Locate every malaria parasite.
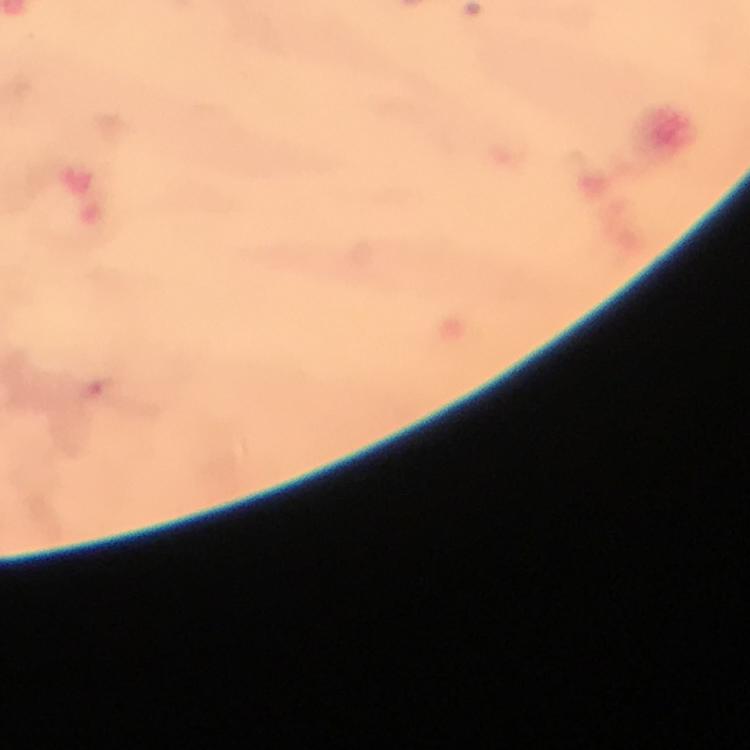

Approximate centers as (x, y) in pixels.
Malaria parasites: (102, 389).

Summary:
  - Magnification: 100x
  - Cropped from: one field of view
  - Preparation: thick blood film
  - Capture: smartphone camera through the microscope
  - Context: from a diagnostic examination for malaria
  - Image size: 750×750 pixels
  - Stain: Giemsa
  - Immersion oil: used